Assess this cell for malaria.
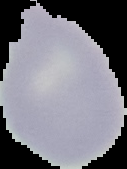
Uninfected.

image type = segmented cell region with the area outside set to black
image size = 127×169 pixels
preparation = thin blood smear